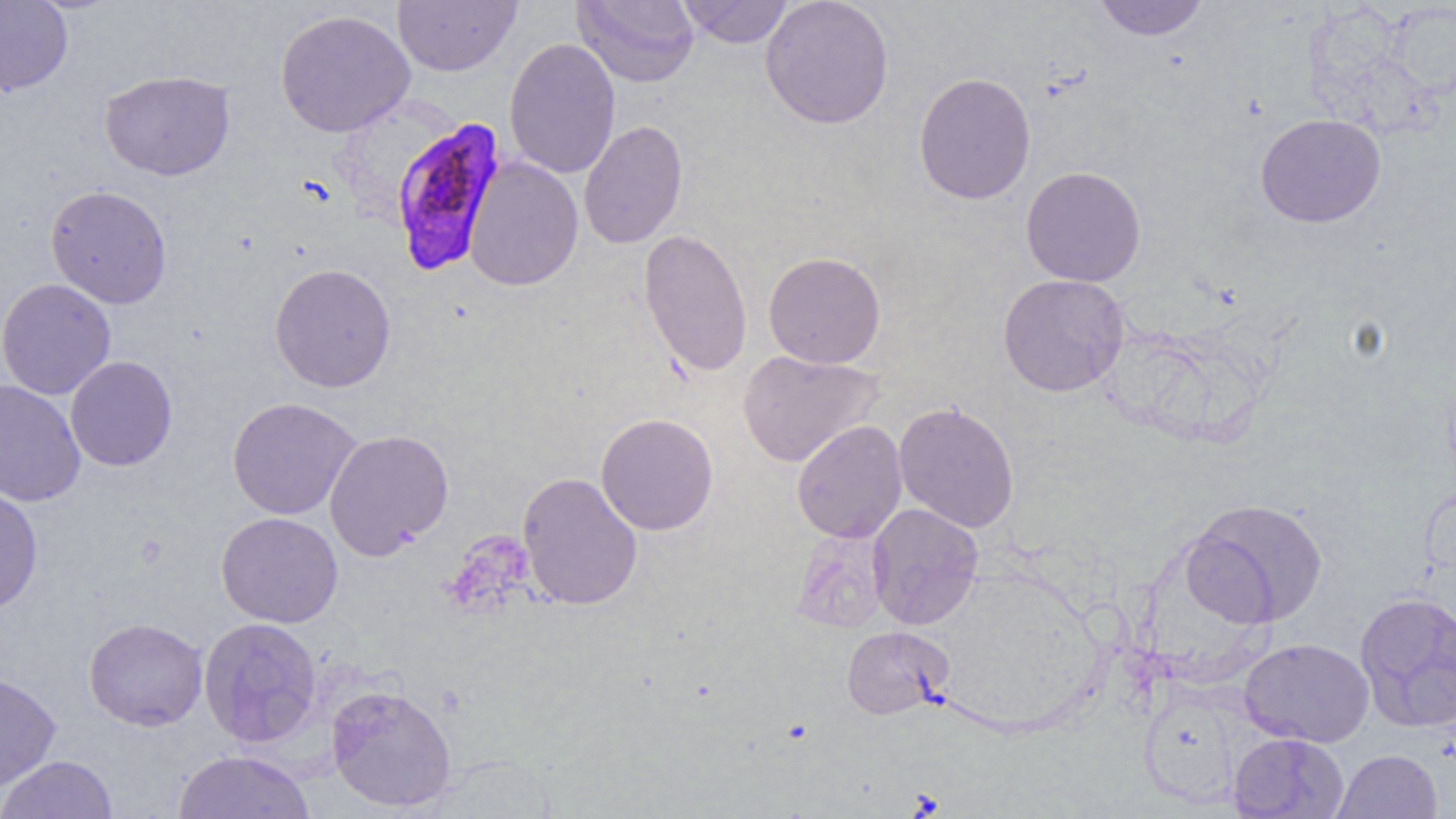

Summary:
  - Coordinate format: approximate bounding boxes as (x1,y1)-(x2,y2) corner pairs in pixels
  - Uninfected red blood cell locations: (392,0)-(521,76), (572,0)-(699,87), (678,0)-(793,48), (760,0)-(894,129), (1093,0)-(1210,40), (0,1)-(73,96), (1385,2)-(1456,98), (274,9)-(415,137), (504,37)-(621,179), (99,69)-(235,181), (914,72)-(1036,204), (1255,113)-(1386,227), (578,120)-(688,248), (463,156)-(583,291), (1021,166)-(1146,287), (46,185)-(172,309), (639,228)-(752,378), (763,251)-(886,369), (269,263)-(397,393), (997,273)-(1130,397), (0,278)-(116,400), (737,350)-(884,468), (65,355)-(177,471), (0,378)-(86,508), (226,397)-(361,520), (893,401)-(1020,533), (596,412)-(719,536), (791,420)-(907,544), (324,428)-(454,560), (517,471)-(643,610), (0,484)-(43,616), (1185,498)-(1328,627), (867,503)-(984,630), (216,512)-(343,628), (791,529)-(890,633), (1354,591)-(1456,732), (84,617)-(208,731), (198,617)-(322,748), (841,625)-(952,719), (1239,638)-(1375,747), (0,670)-(61,791), (1138,677)-(1249,807), (325,683)-(456,812), (1229,732)-(1349,819), (1333,749)-(1443,819), (172,750)-(316,818), (0,755)-(118,819)
  - Plasmodium falciparum-infected red blood cell locations: (389,116)-(508,276)
  - Slide-level diagnosis: Plasmodium falciparum
  - Image size: 1456×819 pixels
  - Modality: optical microscopy
  - Preparation: thin blood smear
  - Field of view: single
  - Magnification: 1000x